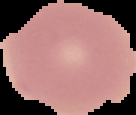
Summary:
  - Preparation: thin blood smear
  - Image type: segmented cell region with the area outside set to black
  - Malaria status: uninfected
  - Image size: 136×115 pixels